Name the blood parasite species.
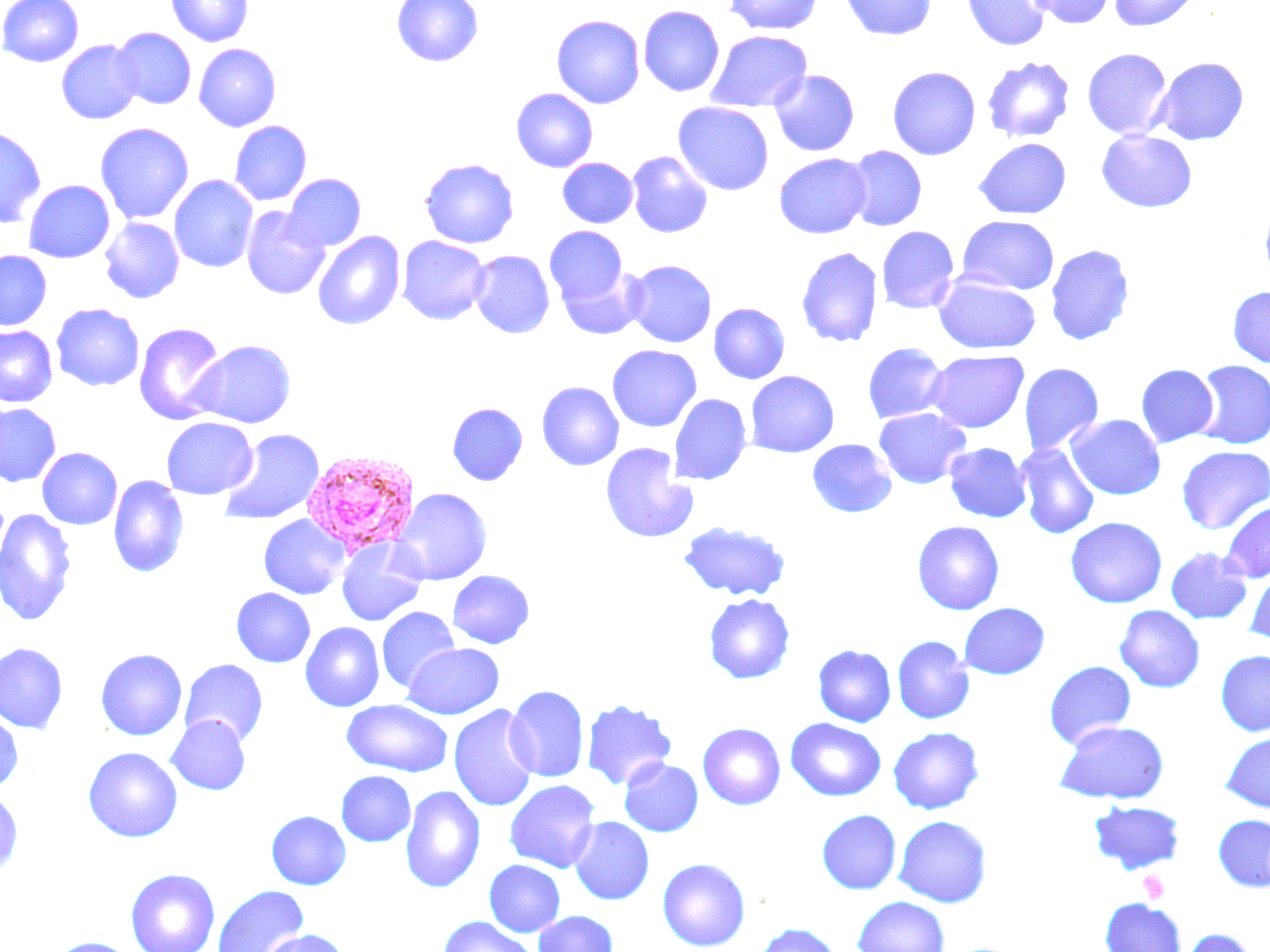
Plasmodium vivax.

uninfected_red_blood_cell_locations: 'approximate bounding boxes as [x1, y1, x2, y2] in pixels: [1, 0, 84, 67], [166, 0, 253, 47], [392, 0, 483, 67], [723, 0, 824, 35], [840, 0, 936, 41], [962, 0, 1051, 51], [1025, 0, 1117, 29], [1108, 0, 1199, 31], [638, 5, 725, 97], [551, 14, 645, 108], [111, 27, 196, 109], [705, 30, 813, 114], [56, 39, 143, 124], [194, 43, 282, 132], [1082, 48, 1172, 139], [981, 55, 1076, 143], [1152, 56, 1249, 146], [887, 66, 981, 160], [770, 69, 860, 156], [511, 88, 598, 172], [673, 102, 774, 195], [229, 121, 312, 205], [94, 122, 195, 224], [0, 125, 46, 228], [1096, 130, 1197, 213], [973, 138, 1071, 220], [844, 146, 927, 232], [626, 150, 714, 239], [774, 153, 871, 239], [420, 158, 519, 248], [557, 158, 638, 228], [284, 173, 366, 250], [169, 175, 258, 273], [23, 180, 115, 263], [1260, 202, 1270, 283], [242, 206, 330, 299], [957, 216, 1059, 295], [99, 217, 185, 304], [544, 226, 628, 306], [876, 226, 960, 314], [313, 231, 405, 330], [397, 235, 490, 325], [1045, 244, 1134, 346], [796, 246, 883, 348], [0, 250, 52, 330], [469, 250, 555, 338], [623, 259, 717, 348], [556, 265, 646, 340], [934, 275, 1041, 355], [1228, 285, 1270, 368], [51, 303, 144, 391], [709, 303, 790, 384], [134, 322, 227, 425], [0, 325, 57, 407], [189, 340, 296, 428], [862, 342, 949, 424], [607, 345, 702, 432], [925, 350, 1028, 432], [1193, 360, 1270, 449], [1018, 362, 1104, 455], [1136, 364, 1219, 447], [745, 371, 840, 458], [536, 381, 624, 471], [669, 394, 752, 486], [447, 402, 528, 485], [0, 403, 61, 486], [873, 408, 971, 489], [1066, 414, 1165, 500], [161, 417, 257, 500], [219, 428, 325, 525], [807, 439, 897, 518], [600, 442, 698, 543], [944, 442, 1032, 523], [1014, 442, 1099, 539], [1176, 445, 1270, 534], [37, 447, 122, 530], [108, 475, 189, 578], [391, 487, 492, 585], [1222, 501, 1270, 582], [0, 509, 77, 626], [258, 514, 350, 599], [1065, 517, 1167, 608], [678, 521, 791, 601], [912, 521, 1004, 615], [337, 538, 428, 626], [1165, 546, 1252, 624], [1244, 566, 1270, 648], [448, 570, 535, 648], [231, 587, 316, 667], [703, 593, 796, 684], [958, 602, 1049, 679], [1114, 605, 1205, 693], [377, 607, 460, 693], [300, 622, 385, 711], [891, 635, 974, 724], [0, 642, 68, 735], [403, 643, 505, 719], [813, 644, 896, 727], [95, 648, 188, 740], [1215, 650, 1270, 736], [179, 659, 269, 748], [1044, 661, 1136, 749], [505, 685, 589, 782], [341, 699, 453, 777], [580, 699, 678, 790], [448, 704, 541, 812], [0, 710, 23, 793], [166, 716, 251, 795], [785, 718, 885, 801], [1055, 721, 1169, 804], [697, 722, 786, 810], [888, 726, 984, 814], [1220, 731, 1270, 813], [83, 747, 183, 842], [620, 758, 703, 836], [336, 771, 416, 846], [504, 779, 601, 873], [400, 785, 486, 893], [0, 791, 23, 879], [1089, 801, 1186, 874], [817, 809, 901, 894], [266, 810, 351, 890], [1213, 814, 1270, 892], [893, 815, 991, 907], [569, 817, 654, 905], [657, 858, 751, 950], [484, 859, 565, 937], [125, 868, 220, 952], [212, 885, 309, 952], [852, 895, 950, 952], [1100, 898, 1186, 952], [532, 910, 618, 952], [437, 916, 540, 952], [752, 923, 842, 952], [1179, 927, 1257, 952], [258, 928, 350, 952], [49, 936, 137, 952]'
image_size: 1270×952 pixels
stain: May-Grünwald-Giemsa
plasmodium_vivax_infected_red_blood_cell_locations: 'approximate bounding boxes as [x1, y1, x2, y2] in pixels: [301, 449, 421, 557]'
preparation: thin blood smear
platelet_locations: 'approximate bounding boxes as [x1, y1, x2, y2] in pixels: [1139, 870, 1170, 904]'
modality: light microscopy
field_of_view: single
magnification: 1000x